Comment on the morphology of the red blood cells.
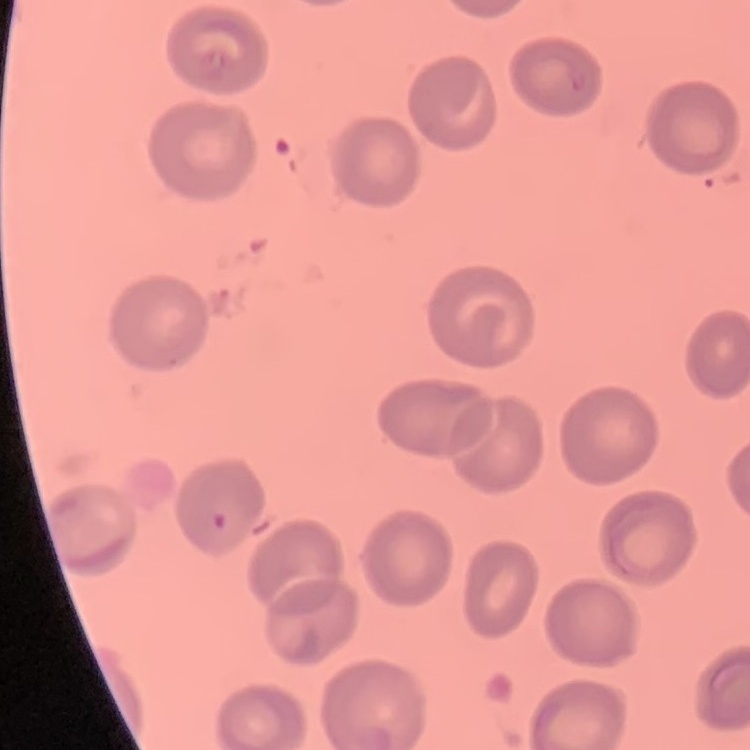

No rouleaux formation.

preparation = thin blood film
image type = one tile cut from a larger photomicrograph
stain = Field's or Giemsa